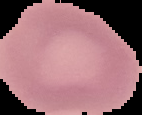

Summary:
  - Preparation: thin blood smear
  - Image size: 142×115 pixels
  - Image type: segmented cell region on a black background
  - Malaria status: uninfected